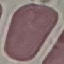 Malaria status: uninfected. Giemsa-stained preparation. Automatically extracted cell patch, resized to 64 × 64 pixels. Thin blood smear. Acquired by smartphone through the microscope eyepiece.